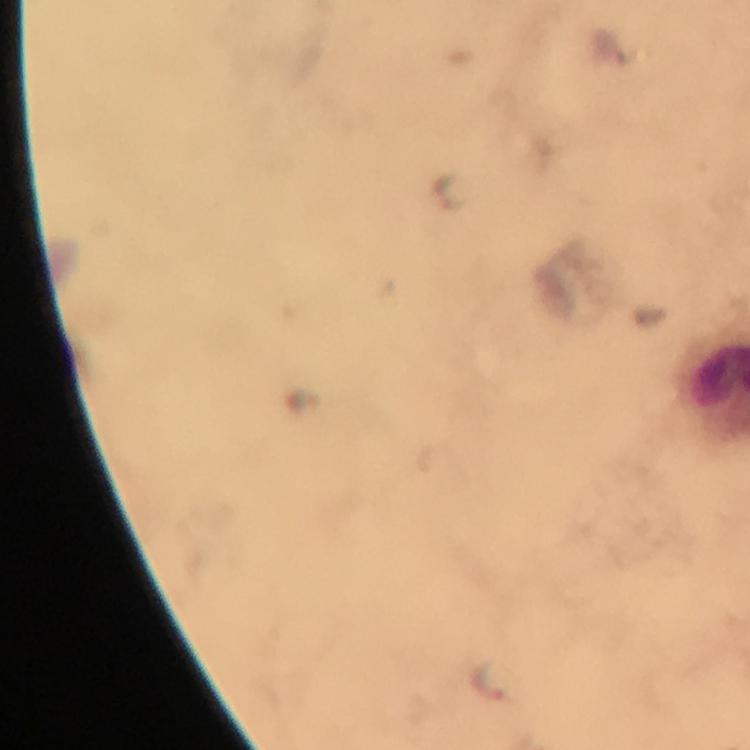
Approximate centers as (x, y) in pixels.
Summary:
  - Malaria parasite locations: (446, 189), (492, 680)
  - Magnification: 100x
  - Context: from a malaria diagnostic workup
  - Cropped from: one field of view
  - Capture: smartphone camera through the microscope
  - Image size: 750×750 pixels
  - Preparation: thick blood film
  - Immersion oil: applied
  - Stain: Giemsa